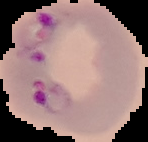

{
  "preparation": "thin blood smear",
  "image_size": "148×142 pixels",
  "image_type": "segmented cell region on a black background",
  "malaria_status": "parasitized"
}